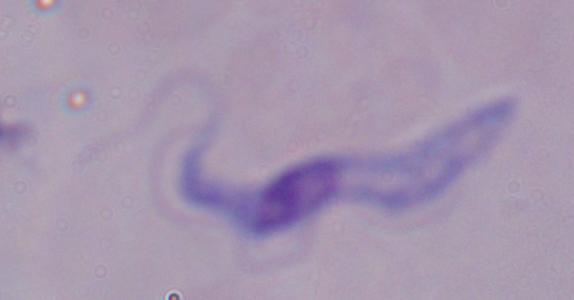
1000x magnification. A trypanosome is seen. Photomicrograph.